Look for parasitized red blood cells.
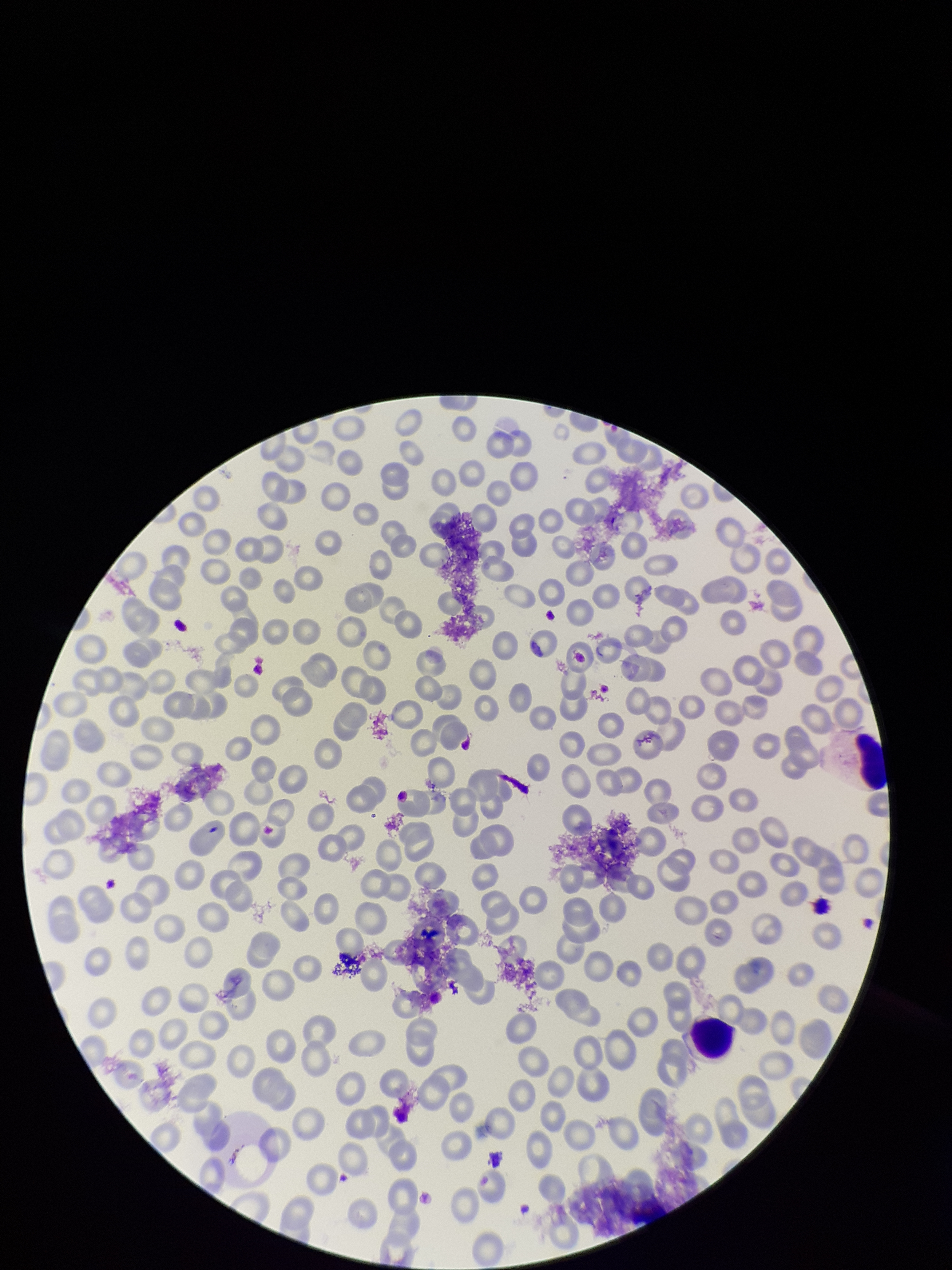
None seen.

Giemsa stain. Preparation: thin. Species reported for this patient: Plasmodium falciparum. Parasitized red blood cell count: 0. Red blood cell count: 196. One field from this slide. Patient malaria status: infected. Smartphone photograph taken through the eyepiece of a microscope. Image is 952×1270 pixels.